Classify this cell by malaria status.
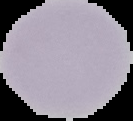

Uninfected.

{
  "preparation": "thin blood smear",
  "image_type": "segmented cell region on a black background",
  "image_size": "133×121 pixels"
}